Locate every Plasmodium falciparum-infected red blood cell.
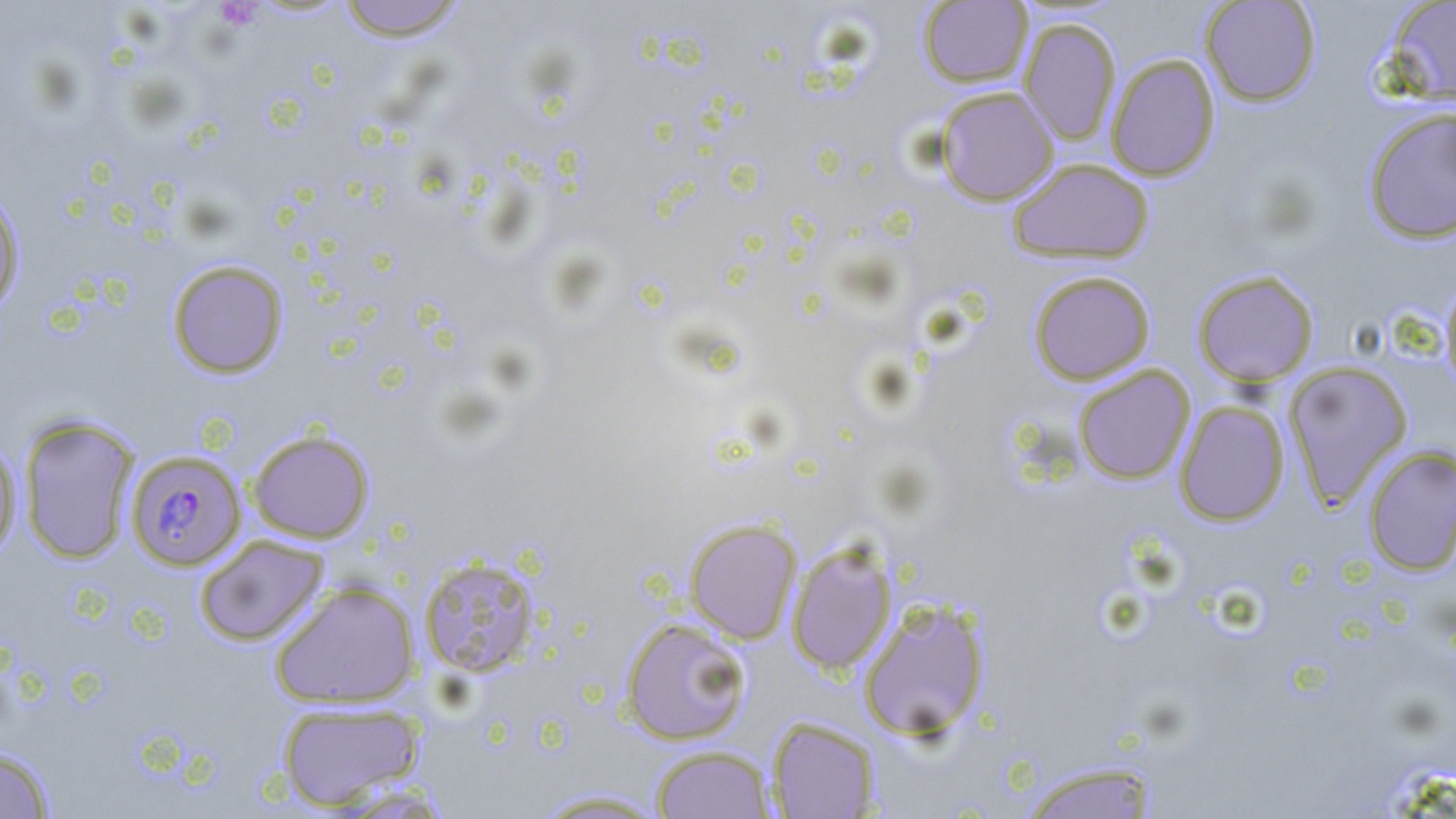
Approximate bounding boxes as named x1/y1/x2/y2 corners in pixels.
Plasmodium falciparum-infected red blood cells: (x1=126, y1=449, x2=246, y2=570).

slide-level diagnosis = Plasmodium falciparum
magnification = 1000x
modality = light microscopy
image size = 1456×819 pixels
stain = May-Grünwald-Giemsa
field of view = one of a larger specimen
uninfected red blood cell locations = approximate bounding boxes as named x1/y1/x2/y2 corners in pixels: (x1=335, y1=0, x2=468, y2=42), (x1=1199, y1=0, x2=1322, y2=106), (x1=1384, y1=0, x2=1456, y2=104), (x1=917, y1=1, x2=1033, y2=87), (x1=1018, y1=17, x2=1122, y2=146), (x1=1106, y1=53, x2=1220, y2=181), (x1=934, y1=86, x2=1059, y2=205), (x1=1362, y1=106, x2=1456, y2=244), (x1=1006, y1=158, x2=1155, y2=264), (x1=0, y1=187, x2=25, y2=317), (x1=166, y1=259, x2=289, y2=378), (x1=1192, y1=269, x2=1320, y2=387), (x1=1028, y1=270, x2=1156, y2=385), (x1=1440, y1=277, x2=1456, y2=399), (x1=1283, y1=361, x2=1414, y2=509), (x1=1073, y1=365, x2=1195, y2=484), (x1=1174, y1=401, x2=1289, y2=526), (x1=17, y1=414, x2=140, y2=564), (x1=246, y1=429, x2=375, y2=544), (x1=0, y1=440, x2=22, y2=562), (x1=1362, y1=445, x2=1456, y2=576), (x1=684, y1=518, x2=802, y2=644), (x1=194, y1=535, x2=329, y2=647), (x1=785, y1=539, x2=899, y2=675), (x1=418, y1=554, x2=543, y2=678), (x1=269, y1=579, x2=421, y2=709), (x1=857, y1=597, x2=991, y2=741), (x1=619, y1=616, x2=752, y2=745), (x1=275, y1=699, x2=426, y2=810), (x1=767, y1=716, x2=881, y2=818), (x1=650, y1=744, x2=776, y2=819), (x1=0, y1=745, x2=56, y2=818), (x1=1018, y1=760, x2=1163, y2=819), (x1=531, y1=788, x2=671, y2=817)
preparation = thin blood smear